Assess the morphology of the erythrocytes.
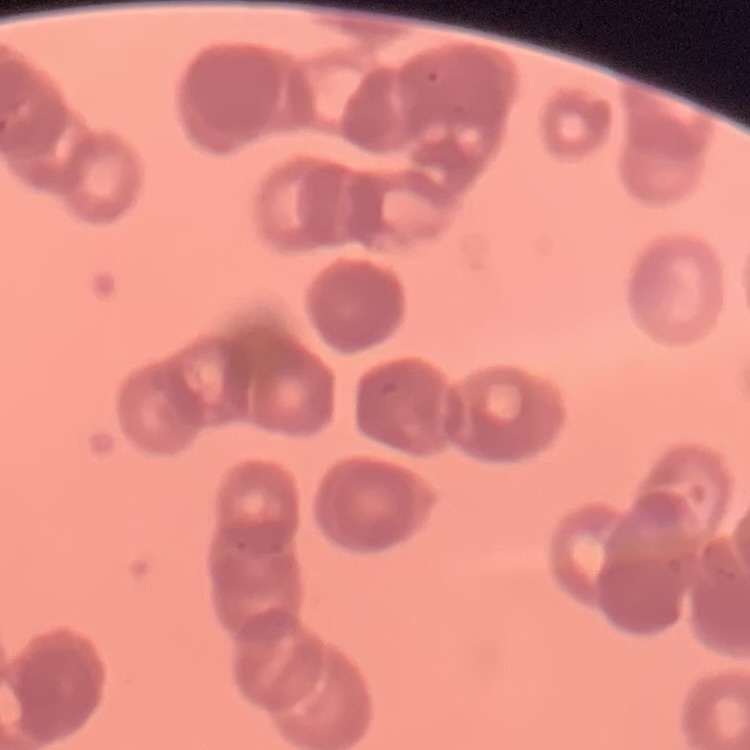
They show rouleaux formation.

Summary:
  - Preparation: thin blood smear
  - Image type: square crop of a larger photomicrograph
  - Stain: Field's or Giemsa